Locate every blood parasite and identify its species.
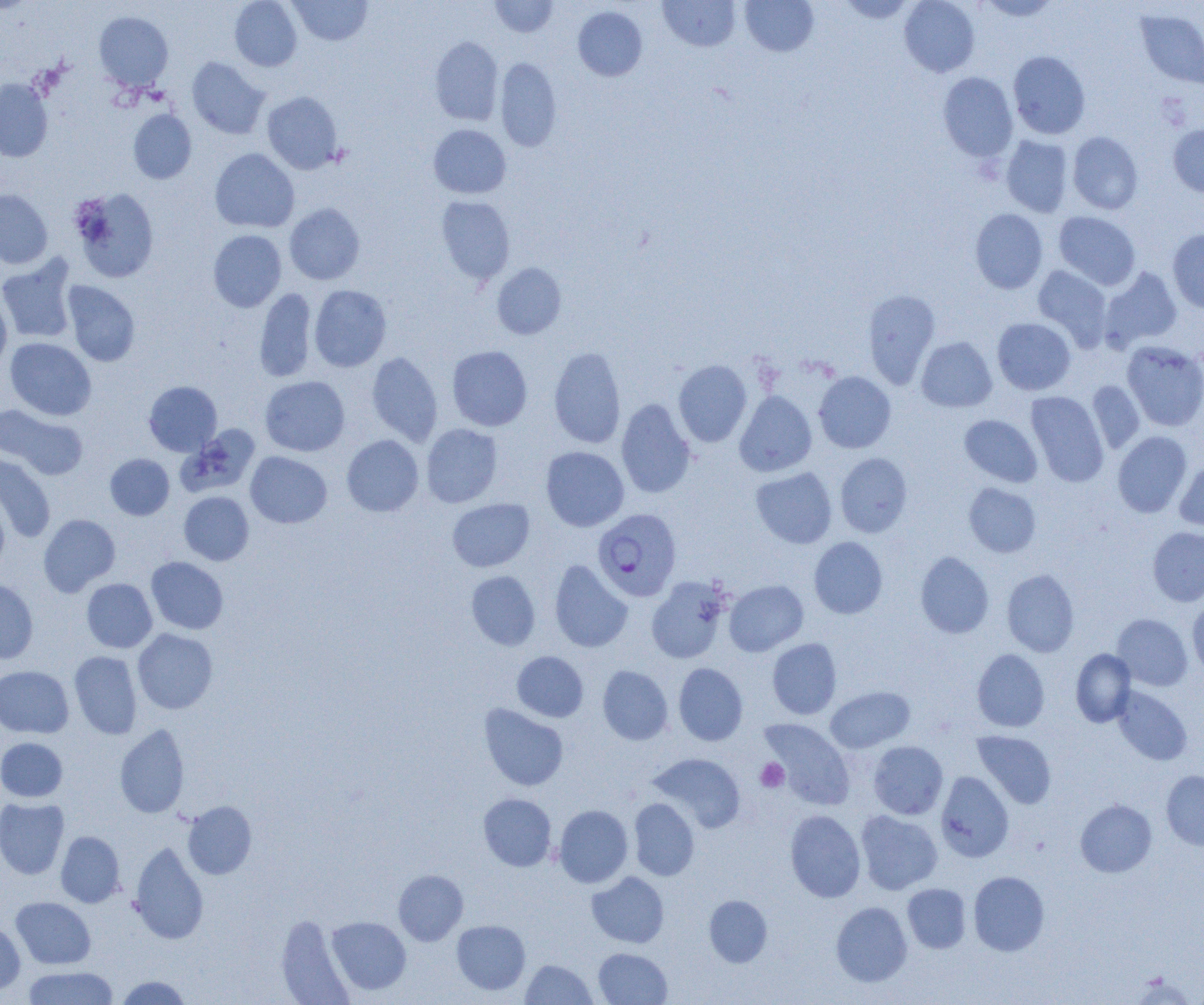
Approximate bounding boxes as [x1, y1, x2, y2] in pixels.
Plasmodium falciparum-infected red blood cells: [593, 508, 681, 601].
No Plasmodium ovale, Plasmodium malariae, Plasmodium vivax, Babesia divergens, or Trypanosoma brucei observed.

Uninfected red blood cell locations: [229, 0, 302, 71], [289, 0, 372, 46], [490, 0, 559, 37], [658, 0, 740, 51], [740, 0, 819, 56], [837, 0, 918, 23], [899, 0, 980, 77], [977, 0, 1062, 21], [573, 6, 647, 81], [1135, 7, 1204, 90], [93, 10, 173, 91], [430, 36, 503, 125], [1008, 50, 1090, 139], [186, 57, 270, 139], [495, 57, 562, 151], [937, 72, 1018, 161], [0, 78, 53, 162], [262, 92, 343, 174], [128, 108, 197, 184], [1168, 122, 1204, 197], [428, 124, 511, 198], [1067, 131, 1143, 215], [1001, 134, 1074, 217], [210, 148, 299, 233], [71, 187, 160, 282], [0, 189, 53, 269], [436, 196, 515, 284], [284, 203, 365, 285], [970, 209, 1048, 294], [1054, 211, 1141, 290], [208, 229, 287, 312], [1167, 229, 1204, 313], [0, 255, 78, 344], [492, 263, 567, 339], [1033, 265, 1113, 351], [1099, 267, 1182, 352], [62, 281, 141, 367], [309, 285, 392, 372], [254, 288, 317, 382], [863, 289, 940, 388], [0, 290, 12, 373], [992, 317, 1076, 395], [4, 337, 96, 420], [917, 337, 996, 412], [1121, 341, 1204, 431], [446, 345, 533, 431], [549, 346, 626, 449], [366, 352, 443, 446], [673, 359, 752, 447], [814, 371, 896, 453], [260, 376, 350, 457], [1087, 380, 1146, 453], [144, 381, 222, 456], [734, 390, 817, 477], [1026, 391, 1108, 487], [616, 398, 696, 499], [1, 404, 88, 481], [959, 415, 1042, 487], [421, 423, 503, 508], [177, 425, 261, 497], [1112, 431, 1192, 518], [341, 434, 424, 517], [540, 446, 629, 531], [245, 451, 332, 528], [0, 453, 56, 542], [835, 453, 913, 537], [105, 454, 174, 520], [1175, 458, 1204, 532], [750, 467, 837, 549], [964, 482, 1041, 557], [0, 489, 10, 576], [179, 491, 254, 565], [447, 498, 535, 572], [38, 514, 120, 596], [1147, 526, 1204, 606], [809, 537, 887, 619], [915, 551, 994, 639], [146, 557, 228, 634], [549, 560, 633, 652], [1002, 569, 1079, 657], [466, 570, 541, 650], [646, 576, 732, 664], [0, 578, 38, 664], [81, 578, 157, 653], [724, 580, 808, 656], [1187, 598, 1204, 682], [1112, 614, 1192, 691], [132, 628, 218, 714], [767, 638, 842, 719], [972, 649, 1049, 732], [1071, 649, 1136, 727], [69, 650, 142, 739], [512, 651, 589, 722], [673, 662, 748, 745], [597, 665, 673, 745], [0, 666, 74, 738], [825, 686, 915, 753], [1112, 686, 1192, 765], [479, 703, 568, 791], [758, 718, 855, 810], [114, 723, 189, 819], [972, 731, 1056, 808], [0, 737, 68, 802], [868, 741, 948, 819], [649, 753, 746, 833], [1161, 770, 1204, 850], [935, 771, 1014, 862], [478, 793, 557, 871], [0, 797, 69, 879], [628, 798, 699, 880], [1075, 799, 1157, 877], [182, 800, 257, 879], [553, 804, 633, 888], [784, 810, 865, 902], [855, 810, 942, 894], [56, 831, 125, 908], [130, 841, 209, 944], [393, 870, 468, 945], [968, 871, 1049, 956], [587, 872, 669, 947], [902, 883, 971, 953], [704, 895, 772, 967], [11, 897, 96, 969], [831, 901, 912, 987], [276, 914, 355, 1005], [326, 916, 411, 996], [0, 920, 25, 995], [452, 920, 530, 995], [593, 948, 672, 1005], [520, 959, 597, 1004], [23, 966, 119, 1005], [1130, 973, 1196, 1005], [114, 975, 192, 1004]. Platelet locations: [755, 758, 789, 792]. Slide-level diagnosis: Plasmodium falciparum. Image is 1204×1005 pixels. Thin blood smear. 1000x magnification. One field of a larger specimen. Optical microscopy.